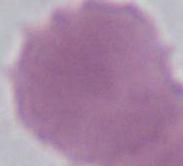

identification: red blood cell
modality: micrograph
magnification: 1000x